State the preparation type.
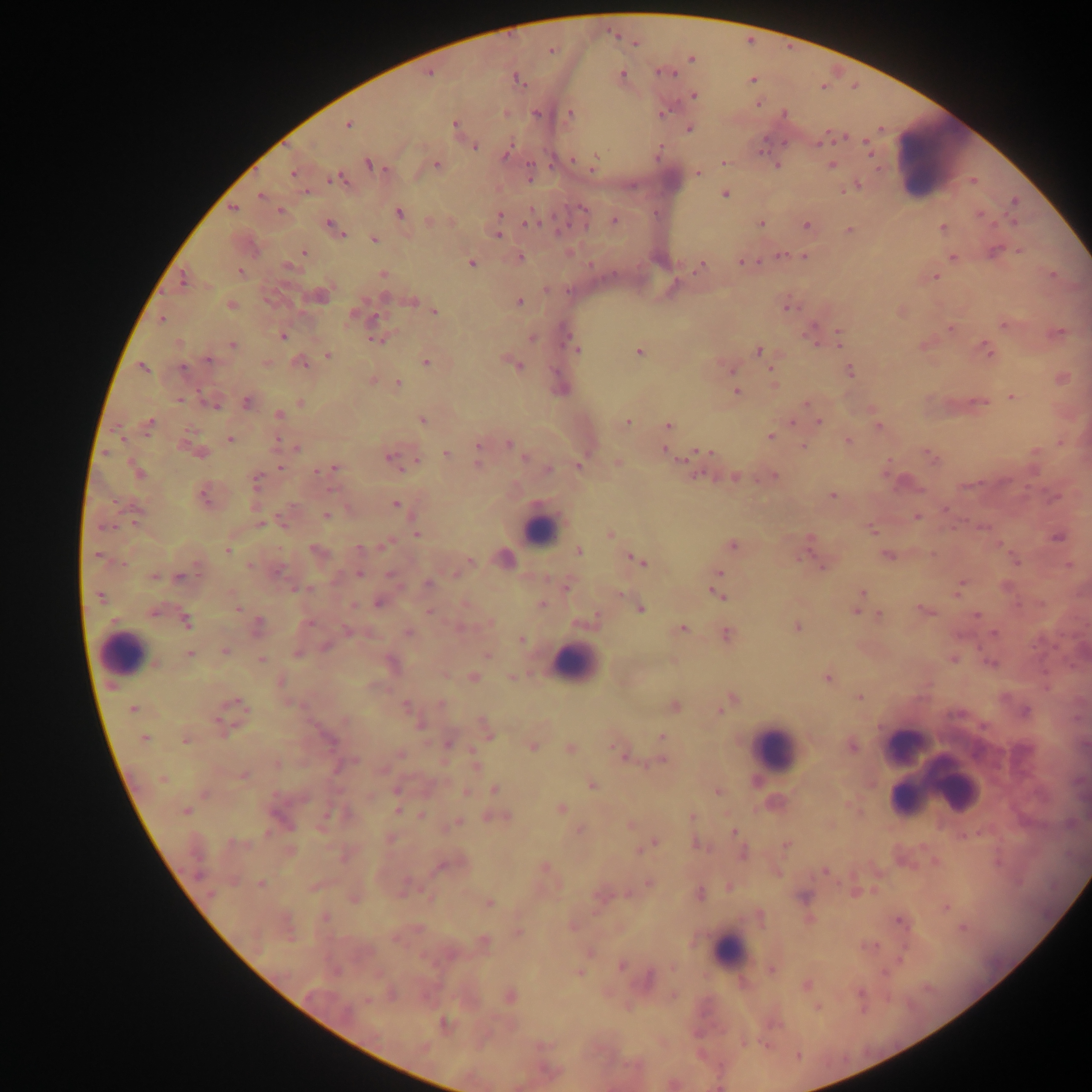

Thick blood film.

Approximate centers as (x, y) in pixels. Leukocyte locations: (938, 160), (540, 529), (123, 653), (575, 664), (904, 745), (774, 748), (947, 780), (904, 799), (730, 951). Malaria parasite locations: (551, 51), (691, 59), (668, 73), (428, 74), (621, 75), (517, 79), (752, 80), (694, 95), (758, 103), (537, 113), (662, 114), (784, 114), (570, 115), (348, 124), (455, 124), (688, 130), (820, 143), (475, 146), (867, 146), (505, 156), (574, 160), (594, 161), (723, 162), (368, 164), (437, 165), (778, 165), (831, 165), (698, 172), (293, 173), (338, 179), (857, 187), (307, 192), (725, 194), (260, 196), (1014, 200), (232, 208), (583, 209), (280, 211), (399, 213), (500, 214), (979, 215), (614, 220), (429, 221), (528, 221), (761, 224), (807, 226), (943, 227), (334, 228), (849, 231), (498, 234), (374, 239), (304, 252), (995, 252), (1019, 252), (781, 255), (804, 257), (953, 257), (520, 258), (742, 261), (471, 263), (288, 267), (699, 267), (241, 272), (383, 273), (936, 277), (183, 279), (385, 298), (412, 301), (520, 302), (231, 305), (789, 307), (435, 312), (352, 316), (374, 318), (162, 320), (1005, 326), (950, 328), (811, 333), (283, 335), (839, 339), (377, 340), (532, 340), (233, 345), (576, 349), (759, 351), (988, 351), (639, 352), (327, 355), (209, 360), (266, 362), (301, 362), (426, 362), (519, 366), (143, 368), (183, 368), (850, 372), (773, 377), (398, 383), (737, 391), (1013, 397), (181, 400), (247, 402), (980, 402), (301, 403), (807, 403), (214, 405), (279, 414), (422, 421), (627, 422), (793, 422), (819, 422), (149, 423), (668, 425), (878, 427), (770, 436), (230, 439), (848, 442), (278, 443), (478, 444), (509, 444), (804, 446), (297, 448), (197, 451), (665, 451), (708, 452), (446, 453), (931, 457), (389, 458), (525, 458), (416, 459), (618, 463), (478, 465), (579, 465), (280, 467), (334, 468), (326, 469), (549, 469), (138, 471), (317, 472), (697, 475), (774, 476), (734, 478), (256, 480), (832, 495), (204, 496), (395, 505), (327, 515), (917, 517), (259, 524), (105, 526), (871, 529), (610, 533), (416, 534), (1058, 538), (385, 545), (732, 546), (359, 547), (316, 550), (227, 551), (578, 551), (97, 554), (886, 555), (801, 556), (470, 560), (640, 561), (1068, 565), (250, 566), (821, 566), (278, 571), (390, 573), (719, 573), (359, 574), (455, 574), (153, 577), (179, 577), (428, 583), (566, 587), (959, 587), (1006, 587), (307, 588), (299, 589), (861, 593), (620, 594), (719, 595), (101, 597), (378, 603), (541, 604), (353, 606), (237, 607), (641, 609), (925, 610), (856, 611), (153, 612), (429, 612), (976, 614), (880, 615), (591, 620), (186, 622), (491, 622), (310, 623), (258, 625), (797, 628), (682, 629), (347, 632), (409, 633), (994, 634), (726, 635), (521, 640), (325, 647), (224, 650), (298, 654), (190, 655), (487, 655), (261, 659), (953, 661), (990, 663), (473, 676), (512, 677), (828, 678), (281, 682), (859, 697), (732, 698), (440, 703), (238, 704), (405, 705), (674, 706), (133, 709), (720, 710), (1025, 711), (420, 724), (222, 727), (488, 734), (662, 737), (145, 738), (186, 740), (329, 741), (448, 744), (532, 746), (853, 747), (570, 748), (618, 750), (400, 754), (354, 760), (660, 761), (277, 764), (475, 764), (337, 767), (244, 776), (162, 779), (591, 784), (396, 790), (495, 790), (466, 792), (718, 792), (561, 808), (398, 810), (184, 811), (421, 815), (327, 816), (692, 817), (499, 818), (458, 822), (631, 824), (580, 831), (734, 831), (655, 843), (237, 844), (698, 845), (786, 845), (649, 846), (743, 853), (440, 867), (545, 867), (826, 872), (648, 883), (261, 884), (729, 887), (700, 893), (804, 897), (489, 903), (946, 907), (326, 917), (900, 921), (963, 928), (519, 932), (485, 941), (901, 959), (622, 966), (771, 970), (580, 972), (806, 986), (511, 996), (367, 1001), (444, 1024). Image is 1092×1092 pixels. Mobile-phone photograph taken through the microscope. One field of view. Sample from Ghana.